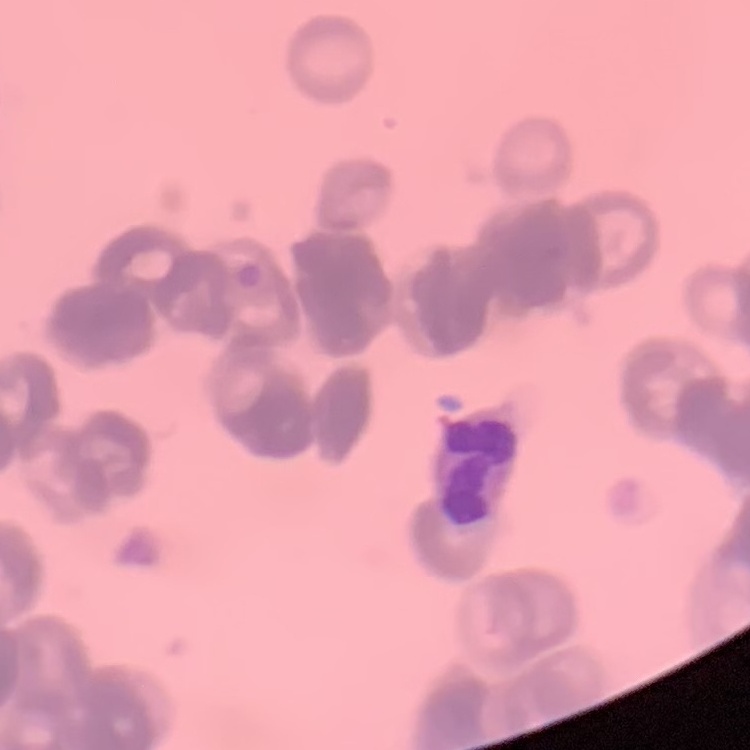

The erythrocytes show rouleaux formation. Thin blood film. One tile cut from a larger photomicrograph. Stained with either Field's or Giemsa.